Classify this cell by malaria status.
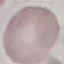
Uninfected.

Photographed with a smartphone camera at the microscope eyepiece. Giemsa stain. Thin blood film. Cell patch, automatically extracted from a larger field of view and resized to 64 × 64 pixels.